Assess the morphology of the erythrocytes.
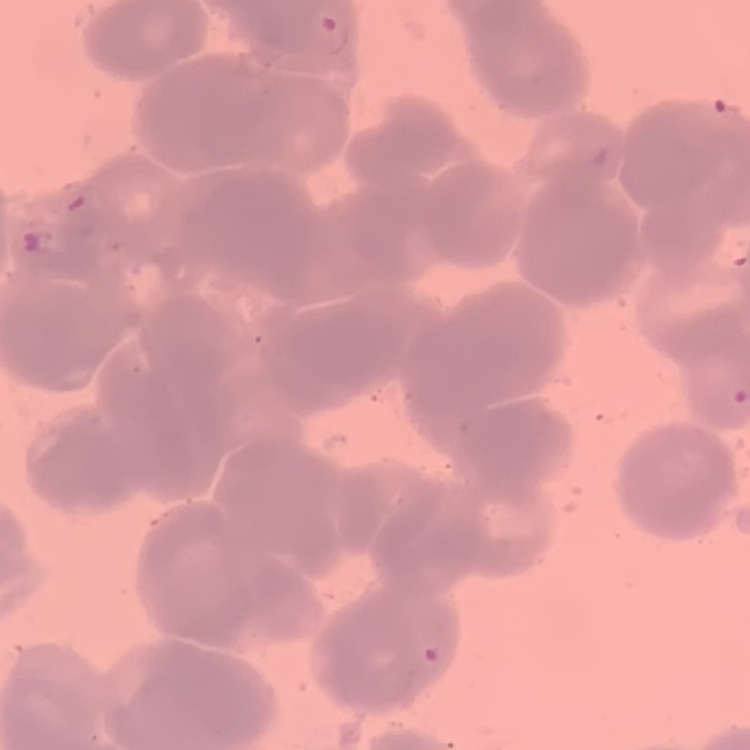
Rouleaux formation.

Square crop of a larger photomicrograph. Thin blood film. Stained with either Field's or Giemsa.